Comment on the morphology of the erythrocytes.
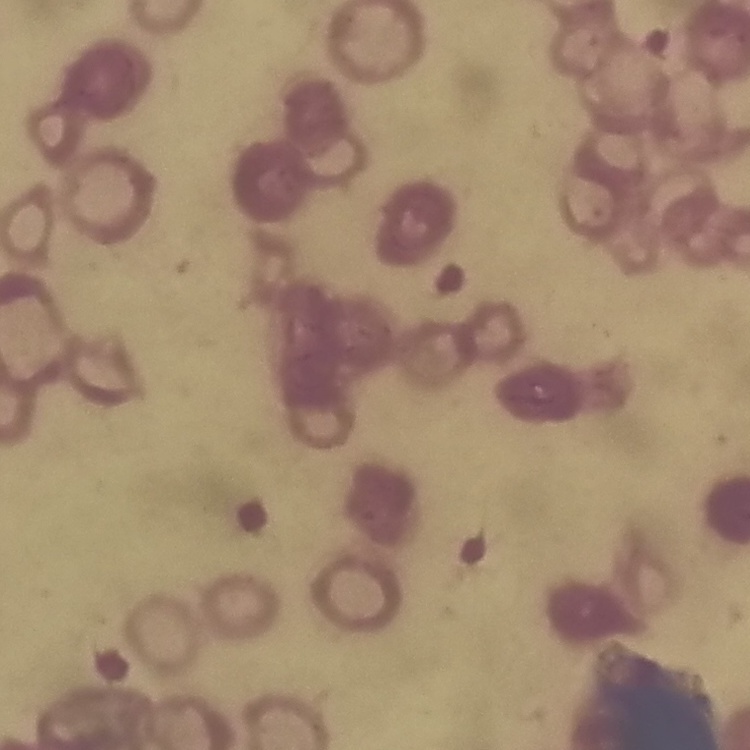

Rouleaux formation.

Thin peripheral smear. Stained with either Field's or Giemsa. One tile cut from a larger photomicrograph.